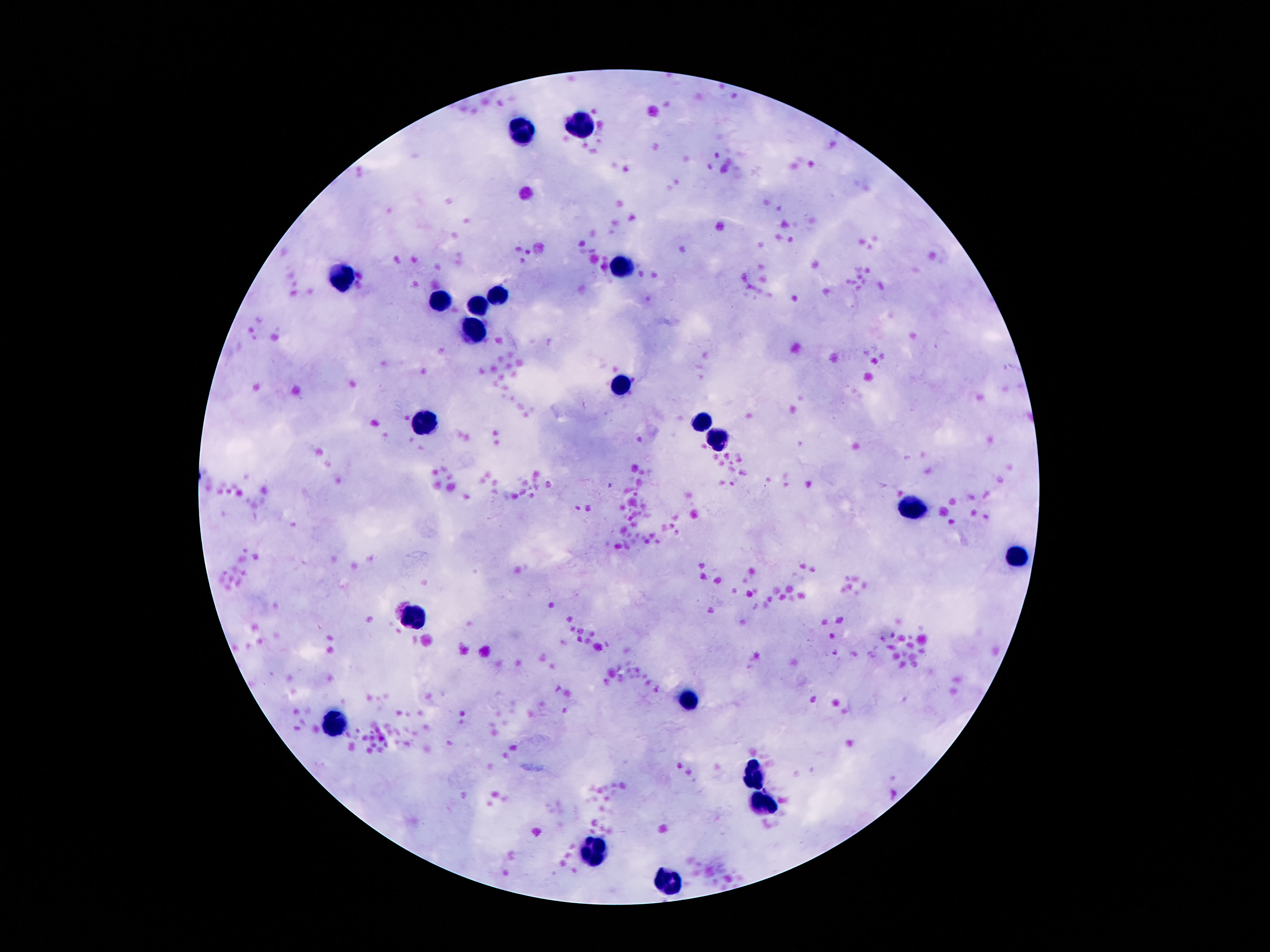
patient malaria status = not infected
preparation = thick blood smear
leukocyte locations = approximate object centers, in pixels from the top-left corner: (x=582, y=123), (x=523, y=132), (x=619, y=266), (x=340, y=278), (x=493, y=294), (x=441, y=303), (x=479, y=306), (x=472, y=331), (x=617, y=385), (x=426, y=421), (x=703, y=422), (x=718, y=438), (x=922, y=506), (x=1016, y=559), (x=416, y=616), (x=687, y=696), (x=338, y=723), (x=750, y=771), (x=764, y=804), (x=592, y=853), (x=670, y=881)
field of view = one from this slide
magnification = 100x
image size = 1270×952 pixels
capture = smartphone camera through the microscope eyepiece
stain = Giemsa